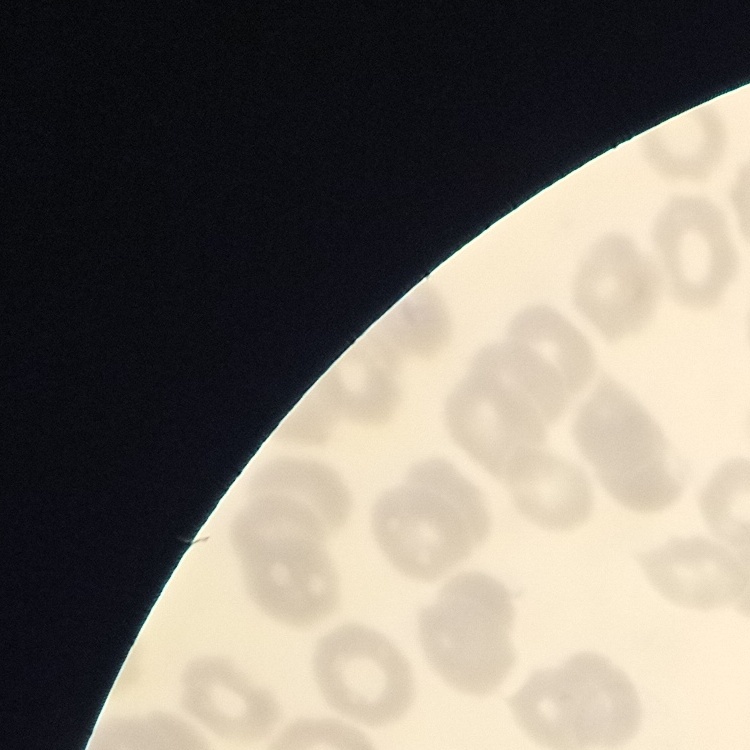
red_blood_cell_morphology: no rouleaux formation
image_type: square crop of a larger photomicrograph
preparation: thin blood film
stain: Field's or Giemsa